Describe the morphology of the erythrocytes.
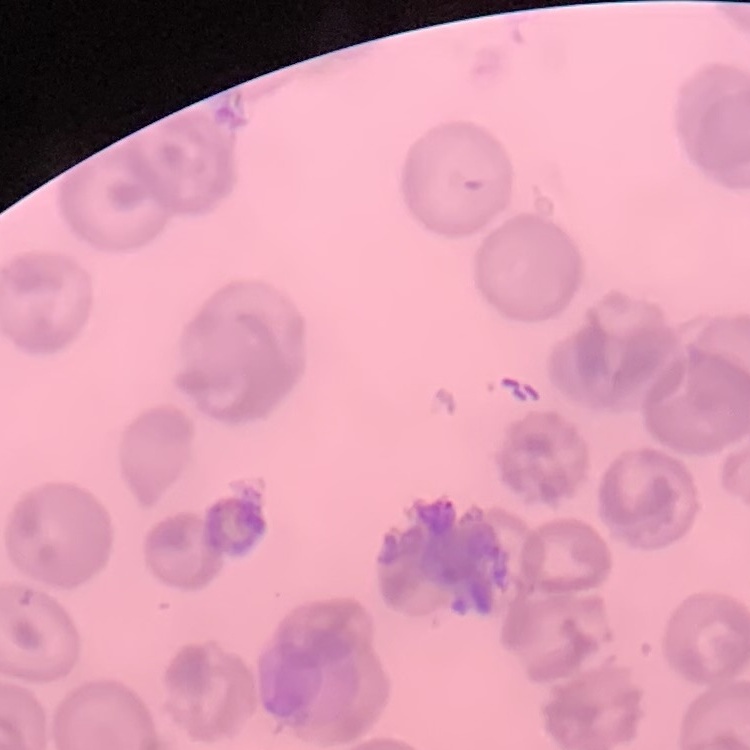

They show no rouleaux formation.

image_type: square crop of a larger photomicrograph
stain: Field's or Giemsa
preparation: thin blood smear